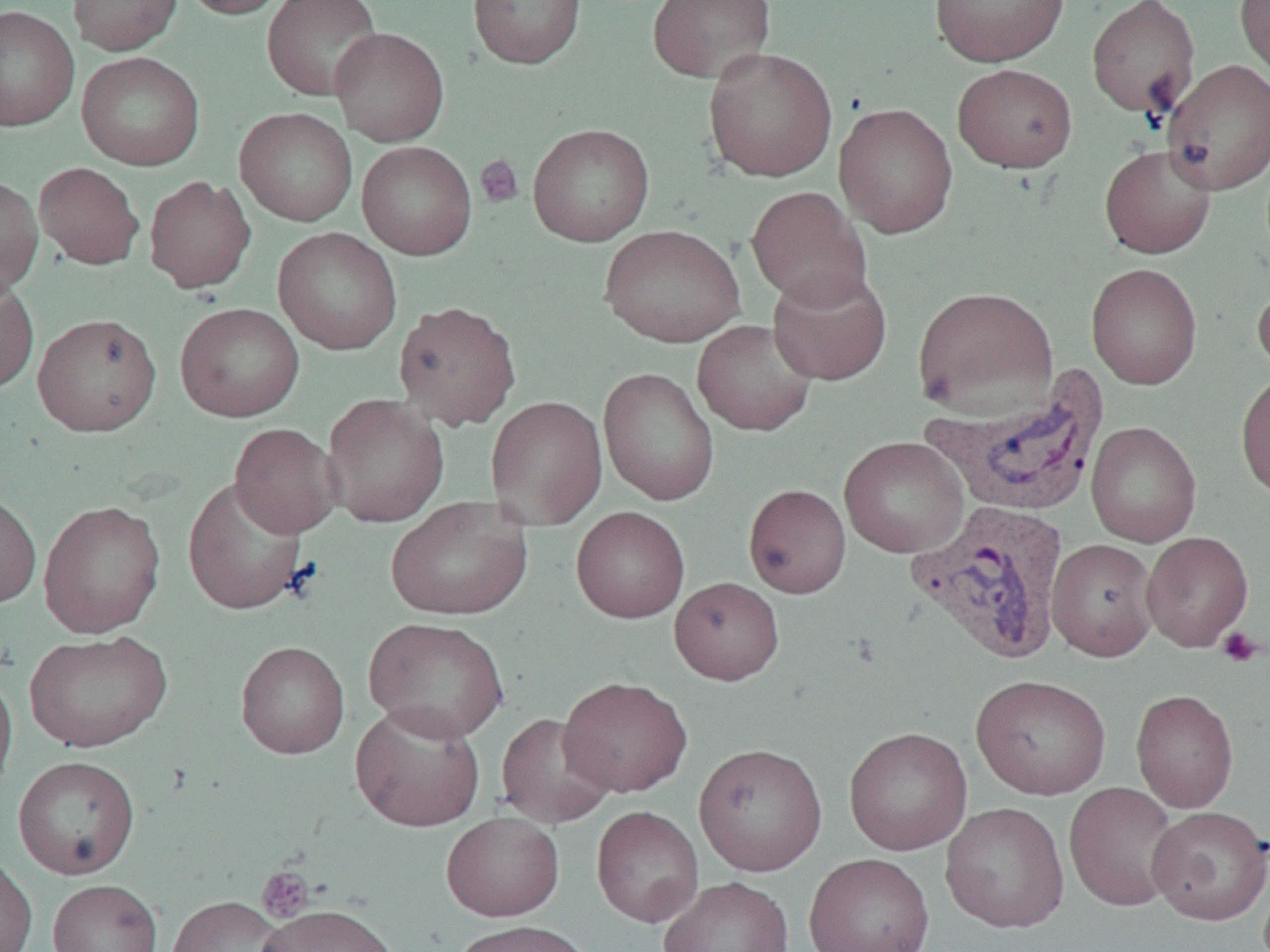

Summary:
  - Coordinate format: approximate bounding boxes as (x1,y1)-(x2,y2) corner pairs in pixels
  - Platelet locations: (475,154)-(524,208), (1216,627)-(1264,668), (257,867)-(315,923)
  - Uninfected red blood cell locations: (68,0)-(183,56), (179,0)-(292,19), (262,0)-(383,101), (467,0)-(587,69), (646,0)-(777,83), (929,0)-(1070,66), (1086,0)-(1200,119), (1235,0)-(1270,80), (0,5)-(79,131), (329,27)-(449,146), (702,46)-(838,182), (76,51)-(205,171), (1162,59)-(1270,195), (952,63)-(1077,173), (834,102)-(958,239), (234,108)-(358,226), (527,123)-(655,246), (356,141)-(477,260), (1099,144)-(1217,259), (34,162)-(144,269), (0,175)-(44,299), (144,176)-(256,294), (746,186)-(871,309), (599,224)-(746,348), (272,227)-(403,355), (1086,263)-(1202,390), (767,267)-(892,385), (0,274)-(40,394), (1253,277)-(1270,383), (913,286)-(1058,416), (392,300)-(522,431), (175,302)-(305,423), (32,312)-(161,436), (693,319)-(818,436), (598,366)-(720,506), (1235,371)-(1270,501), (321,393)-(449,527), (485,395)-(608,530), (1086,421)-(1202,548), (229,423)-(341,538), (839,436)-(969,558), (182,476)-(308,615), (743,484)-(851,598), (0,491)-(41,609), (386,497)-(533,620), (38,499)-(166,638), (571,506)-(690,623), (1141,531)-(1253,651), (1047,538)-(1159,661), (669,577)-(785,685), (364,617)-(509,742), (24,629)-(172,753), (235,640)-(350,759), (0,669)-(17,801), (971,674)-(1111,800), (558,676)-(692,797), (1131,688)-(1239,812), (351,701)-(485,832), (496,712)-(617,828), (844,726)-(972,855), (693,742)-(828,876), (13,755)-(141,879), (1064,782)-(1182,911), (940,801)-(1069,933), (1147,804)-(1270,925), (591,806)-(704,927), (441,812)-(565,921), (803,852)-(935,952), (0,855)-(38,952), (659,876)-(793,952), (48,879)-(162,952), (166,895)-(290,952), (256,903)-(401,952), (450,920)-(598,952)
  - Plasmodium vivax-infected red blood cell locations: (919,361)-(1114,519), (905,501)-(1069,664)
  - Slide-level diagnosis: Plasmodium vivax
  - Magnification: 1000x
  - Preparation: thin blood smear
  - Field of view: one of a larger specimen
  - Modality: light microscopy
  - Image size: 1270×952 pixels